Give the position of every malaria parasite.
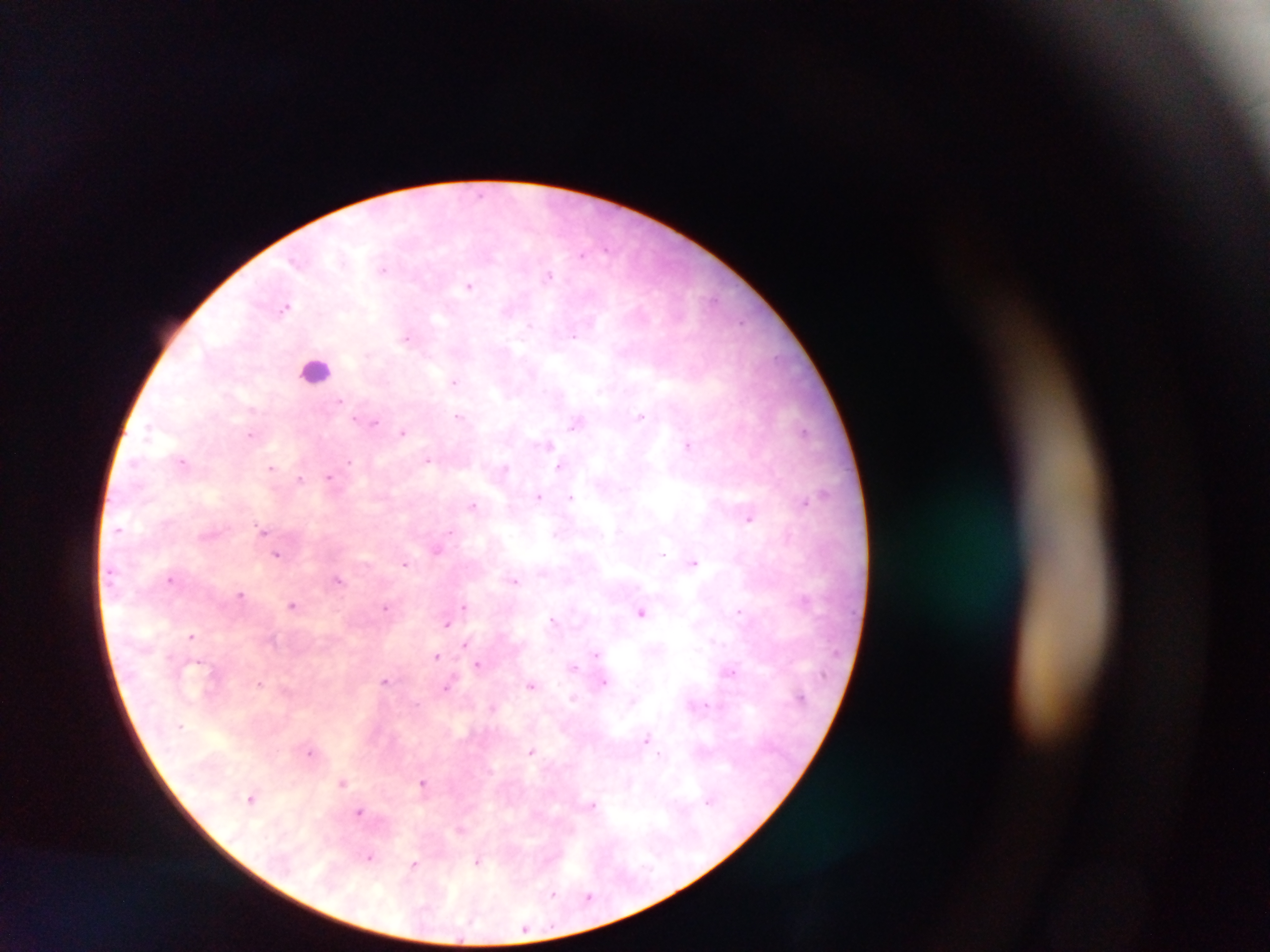

Approximate centers as x y in pixels.
Malaria parasites: 583 254; 384 268; 548 274; 468 286; 286 306; 409 337; 456 382; 641 416; 459 417; 577 423; 403 432; 804 432; 252 434; 547 444; 688 444; 428 459; 183 461; 562 465; 272 467; 330 477; 299 480; 824 494; 539 496; 571 497; 805 503; 474 504; 750 517; 120 529; 264 533; 268 537; 436 549; 661 552; 278 555; 694 562; 405 563; 172 579; 338 580; 514 580; 242 595; 805 600; 293 604; 465 605; 388 606; 740 611; 641 612; 555 619; 447 622; 192 636; 465 644; 597 654; 437 656; 479 665; 574 667; 731 670; 386 680; 604 682; 259 683; 532 685; 448 686; 647 740; 310 751; 532 751; 343 781; 424 784; 253 798; 711 800; 360 812; 462 829; 371 857; 479 861; 415 864; 553 894; 589 896; 525 928.

Leukocyte locations: 315 369. Image is 1270×952 pixels. Collected in Ghana. Mobile-phone photograph taken through the microscope. Thick blood smear. One field of view.